Classify this cell by malaria status.
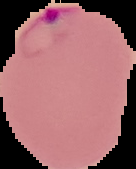
Parasitized.

Summary:
  - Preparation: thin blood film
  - Image size: 136×169 pixels
  - Image type: cell region segmented out of the field of view; surrounding area masked to black